Point out each malaria parasite.
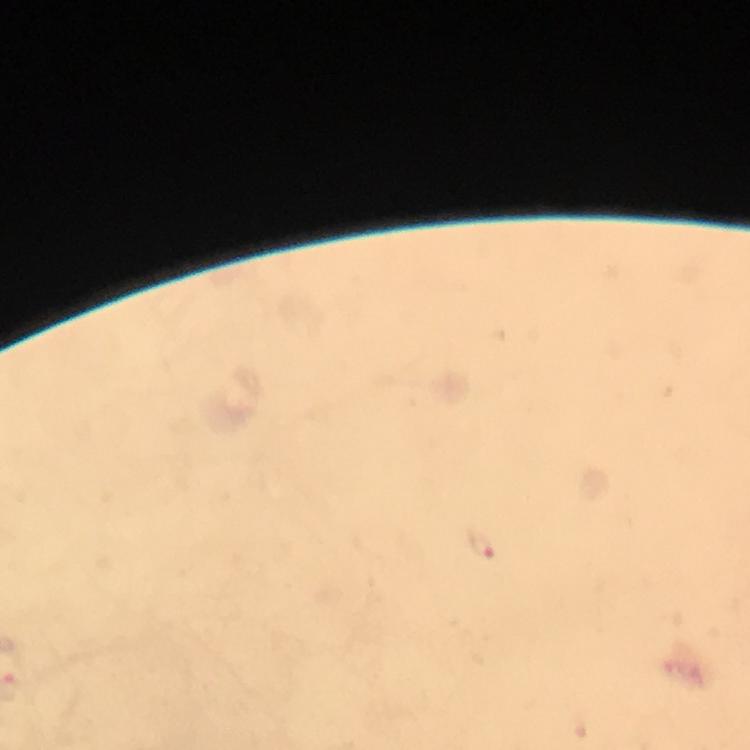

Approximate centers as {x, y} in pixels.
Malaria parasites: {482, 544}.

Summary:
  - Magnification: 100x
  - Context: from a diagnostic examination for malaria
  - Cropped from: one field of view
  - Image size: 750×750 pixels
  - Capture: smartphone mounted on the microscope
  - Stain: Giemsa
  - Immersion oil: applied
  - Preparation: thick smear